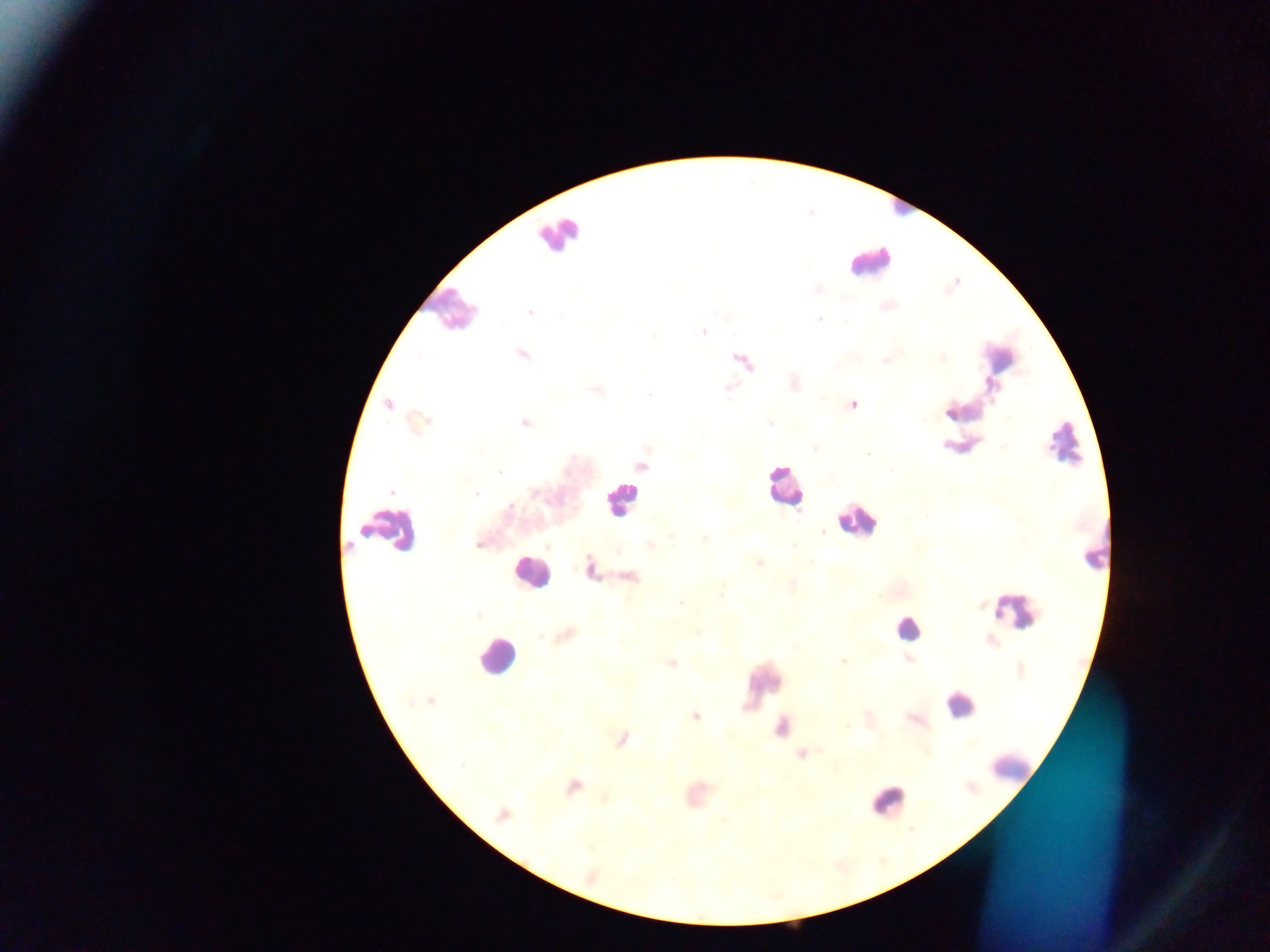
Approximate centers as [x, y] in pixels.
Summary:
  - Leukocyte locations: [557, 234], [868, 260], [451, 308], [998, 356], [1063, 444], [784, 488], [621, 499], [857, 521], [393, 528], [528, 571], [1012, 612], [907, 628], [495, 656], [763, 682], [959, 704], [1013, 769], [888, 800]
  - Malaria parasite locations: [818, 289], [530, 312], [819, 319], [702, 332], [654, 336], [522, 354], [943, 358], [885, 360], [596, 390], [650, 395], [389, 404], [853, 405], [525, 423], [421, 424], [770, 424], [815, 449], [867, 454], [641, 465], [500, 472], [391, 492], [477, 493], [511, 505], [823, 532], [671, 538], [705, 539], [478, 544], [650, 546], [793, 547], [760, 563], [591, 569], [631, 577], [792, 583], [681, 603], [477, 615], [697, 633], [540, 636], [568, 636], [908, 658], [843, 661], [672, 663], [430, 700], [695, 716], [914, 720], [622, 739], [801, 753], [461, 766], [572, 786], [502, 815], [591, 877]
  - Capture: mobile-phone photograph through a microscope
  - Preparation: thick blood smear
  - Image size: 1270×952 pixels
  - Country: Ghana
  - Field of view: single